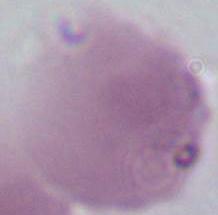

magnification = 1000x
identification = red blood cell
modality = photomicrograph